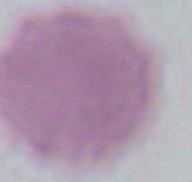

1000x magnification. A red blood cell is shown. Photomicrograph.